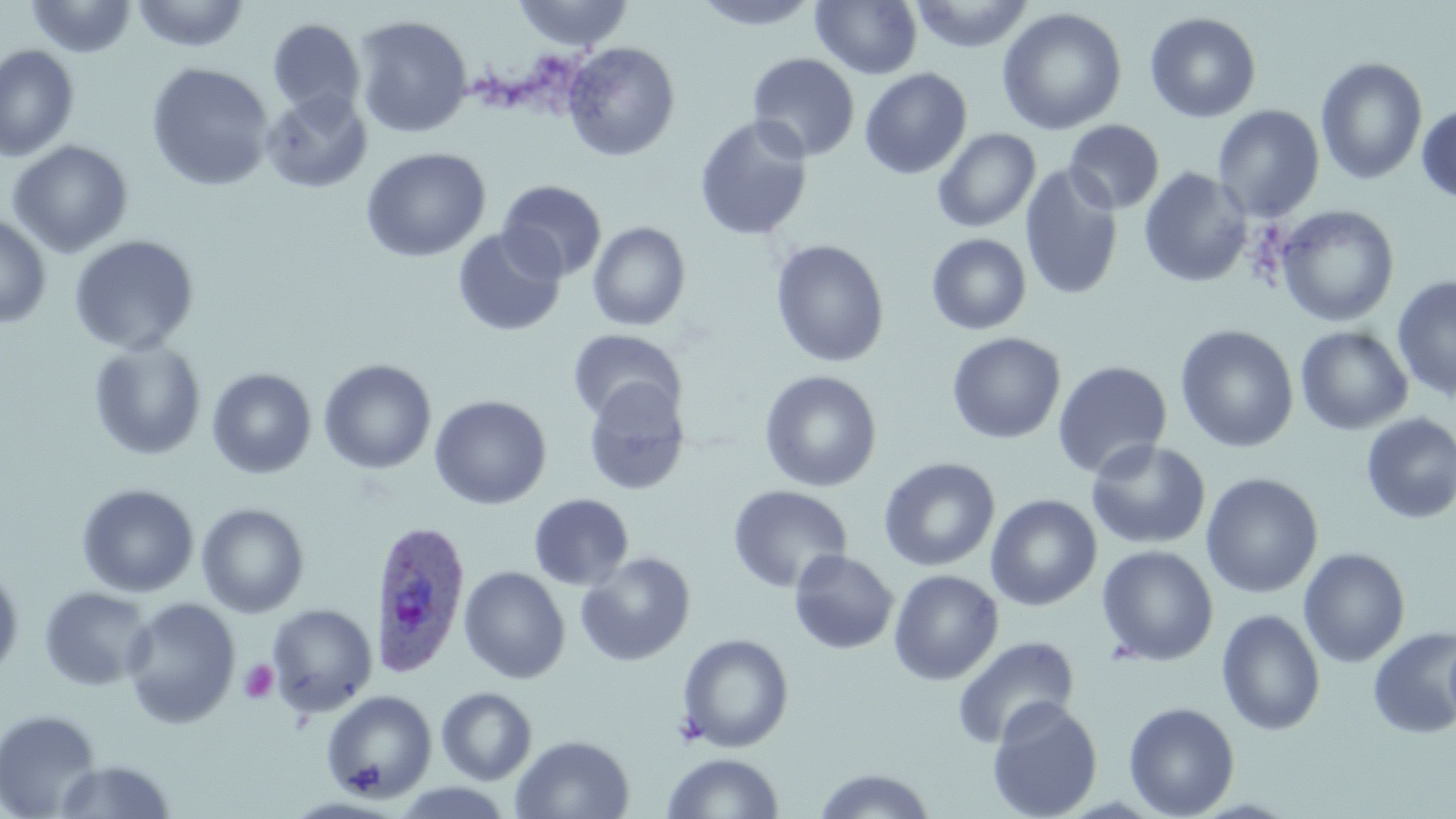
slide-level diagnosis = Plasmodium ovale
stain = May-Grünwald-Giemsa
field of view = single
magnification = 1000x
preparation = thin blood film
image size = 1456×819 pixels
platelet locations = approximate bounding boxes as (x1,y1)-(x2,y2) corner pairs in pixels: (238,659)-(279,705)
uninfected red blood cell locations = approximate bounding boxes as (x1,y1)-(x2,y2) corner pairs in pixels: (26,0)-(137,58), (131,0)-(251,53), (511,0)-(634,52), (692,1)-(820,30), (811,1)-(922,80), (909,1)-(1035,53), (996,7)-(1127,135), (1144,11)-(1262,123), (353,16)-(473,138), (268,19)-(366,118), (562,41)-(681,161), (0,44)-(79,162), (3,46)-(99,259), (746,53)-(860,162), (1315,56)-(1428,186), (145,62)-(275,191), (859,67)-(972,179), (260,89)-(373,194), (1416,104)-(1456,204), (1212,105)-(1325,222), (693,115)-(814,242), (1064,120)-(1165,214), (933,128)-(1041,233), (7,140)-(134,259), (360,147)-(491,263), (1019,163)-(1124,301), (1031,164)-(1237,284), (1138,167)-(1252,288), (496,180)-(607,282), (1276,205)-(1400,327), (0,213)-(52,329), (587,221)-(691,331), (452,227)-(567,337), (926,233)-(1032,335), (68,235)-(199,355), (769,239)-(890,368), (1392,274)-(1456,402), (1175,325)-(1299,453), (1295,326)-(1413,435), (568,329)-(686,426), (946,332)-(1066,444), (88,339)-(207,460), (319,358)-(437,474), (1052,360)-(1173,480), (206,367)-(317,480), (759,370)-(882,492), (582,378)-(691,496), (429,394)-(552,510), (1360,412)-(1456,524), (1085,439)-(1211,550), (878,457)-(1000,572), (1200,472)-(1323,599), (76,483)-(200,597), (727,484)-(852,594), (528,493)-(634,591), (985,494)-(1102,611), (196,502)-(310,618), (1096,544)-(1219,666), (1298,547)-(1411,668), (788,549)-(899,654), (575,552)-(696,666), (0,562)-(24,680), (458,565)-(571,684), (888,569)-(1004,686), (39,586)-(154,691), (120,597)-(241,729), (266,603)-(377,718), (1216,608)-(1326,736), (1367,626)-(1456,739), (1442,630)-(1456,738), (677,633)-(794,753), (951,635)-(1080,750), (436,686)-(538,785), (321,690)-(437,801), (986,697)-(1104,819), (1123,701)-(1239,818), (0,708)-(102,819), (510,734)-(634,818), (662,752)-(783,818), (52,759)-(178,818), (811,767)-(937,818), (388,782)-(519,818)
modality = light microscopy
Plasmodium ovale-infected red blood cell locations = approximate bounding boxes as (x1,y1)-(x2,y2) corner pairs in pixels: (370,520)-(471,677)